Comment on the morphology of the erythrocytes.
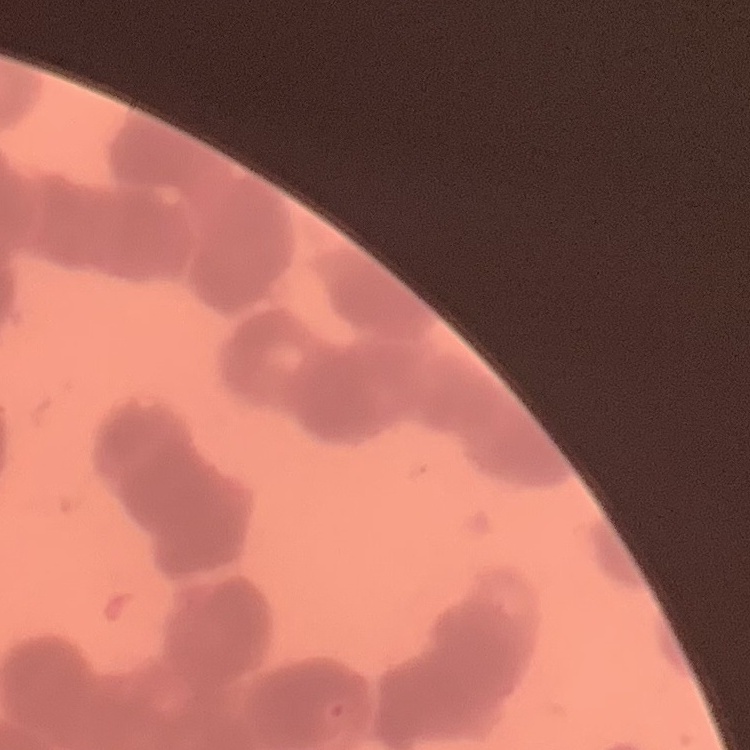
Rouleaux formation.

{
  "preparation": "thin peripheral smear",
  "image_type": "one tile cut from a larger photomicrograph",
  "stain": "Field's or Giemsa"
}